Assess this cell for malaria.
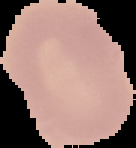
Uninfected.

preparation = thin blood smear
image type = segmented cell region on a black background
image size = 136×148 pixels